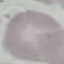

{
  "result": "no malaria parasites seen",
  "stain": "Giemsa",
  "capture": "smartphone through the microscope eyepiece",
  "image_type": "cell patch, automatically extracted from a larger field of view and resized to 64 × 64 pixels",
  "preparation": "thin smear"
}